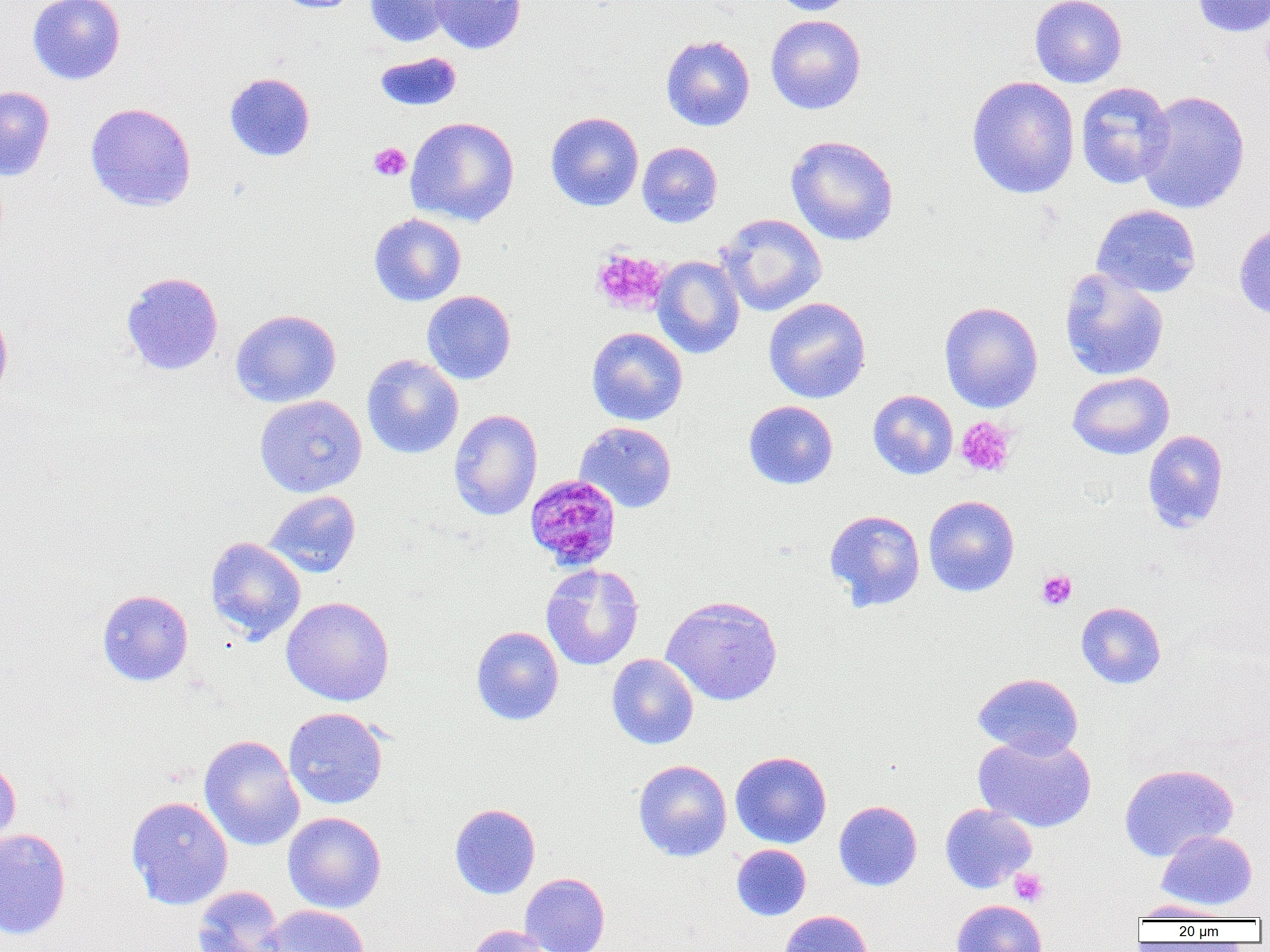
slide-level diagnosis = Plasmodium malariae
image size = 1270×952 pixels
uninfected red blood cell locations = approximate bounding boxes as (x1, y1, x2, y2) in pixels: (27, 0, 126, 85), (273, 0, 364, 13), (365, 0, 455, 48), (429, 0, 526, 54), (771, 0, 858, 16), (1030, 0, 1127, 88), (1191, 0, 1270, 38), (765, 14, 867, 114), (660, 34, 755, 132), (374, 52, 462, 111), (224, 72, 315, 161), (966, 76, 1080, 199), (1075, 81, 1175, 189), (0, 85, 55, 181), (1137, 90, 1250, 215), (85, 102, 197, 212), (545, 111, 644, 211), (405, 116, 520, 226), (785, 134, 899, 246), (637, 141, 722, 228), (1091, 204, 1202, 298), (368, 213, 467, 306), (718, 213, 827, 316), (1234, 221, 1270, 319), (652, 256, 745, 359), (1059, 269, 1169, 381), (121, 271, 224, 376), (422, 290, 516, 384), (763, 297, 871, 403), (939, 301, 1043, 413), (0, 303, 13, 402), (230, 309, 342, 407), (586, 327, 688, 426), (362, 354, 464, 458), (1067, 371, 1174, 459), (868, 390, 958, 479), (254, 394, 367, 497), (743, 400, 838, 490), (448, 409, 543, 521), (575, 421, 677, 513), (1143, 430, 1229, 532), (263, 490, 361, 578), (923, 495, 1020, 597), (825, 509, 925, 611), (205, 536, 306, 644), (541, 563, 644, 671), (97, 589, 193, 686), (661, 595, 783, 706), (281, 596, 395, 706), (1076, 601, 1166, 689), (471, 626, 564, 726), (606, 653, 699, 749), (972, 672, 1083, 759), (283, 707, 389, 809), (974, 733, 1096, 832), (199, 735, 304, 851), (730, 751, 832, 848), (0, 757, 21, 852), (633, 759, 732, 861), (1119, 763, 1238, 861), (125, 796, 233, 910), (834, 800, 922, 891), (450, 803, 540, 899), (939, 803, 1037, 893), (283, 812, 386, 913), (0, 828, 72, 941), (1157, 830, 1257, 910), (731, 844, 811, 920), (520, 873, 610, 952), (191, 885, 285, 952), (952, 899, 1046, 952), (1131, 900, 1230, 920), (262, 904, 370, 952), (780, 910, 873, 952), (466, 925, 553, 952)
Plasmodium malariae-infected red blood cell locations = approximate bounding boxes as (x1, y1, x2, y2) in pixels: (524, 474, 622, 572)
platelet locations = approximate bounding boxes as (x1, y1, x2, y2) in pixels: (369, 142, 411, 181), (591, 248, 668, 315), (955, 416, 1016, 477), (1037, 570, 1077, 610), (1009, 868, 1048, 906)
modality = optical microscopy
field of view = one of a larger specimen
magnification = 1000x
preparation = thin blood smear